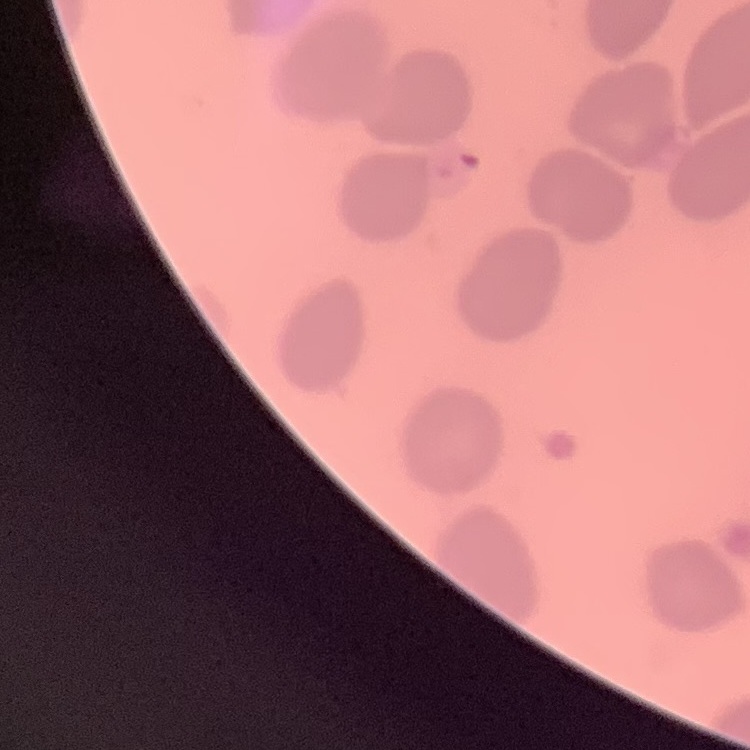
Summary:
  - Red blood cell morphology: no rouleaux formation
  - Image type: square crop of a larger photomicrograph
  - Preparation: thin peripheral smear
  - Stain: Field's or Giemsa